Locate malaria parasites and leukocytes.
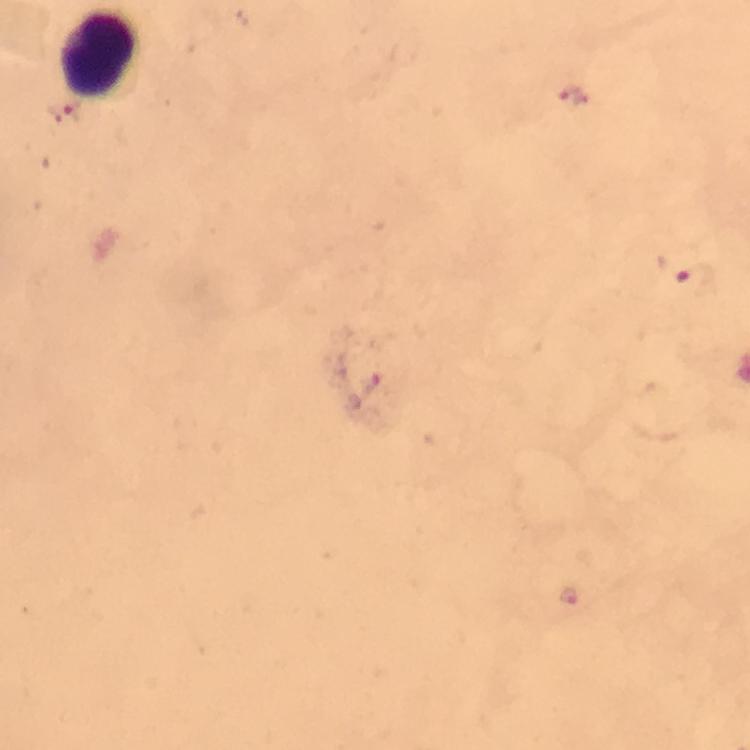

Approximate object centers, in pixels from the top-left corner.
Malaria parasites: (x=571, y=94), (x=695, y=277), (x=569, y=595).
Leukocytes: (x=96, y=55).

Summary:
  - Immersion oil: applied
  - Image size: 750×750 pixels
  - Stain: Giemsa
  - Capture: smartphone photograph through a microscope
  - Preparation: thick blood film
  - Cropped from: a single field of view
  - Magnification: 100x
  - Context: from a diagnostic examination for malaria